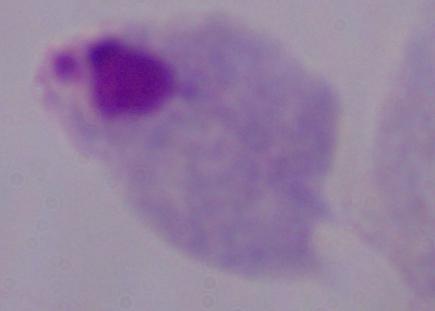 1000x magnification. A trichomonad is shown. Micrograph.